Give the extent of all uninfected red blood cells.
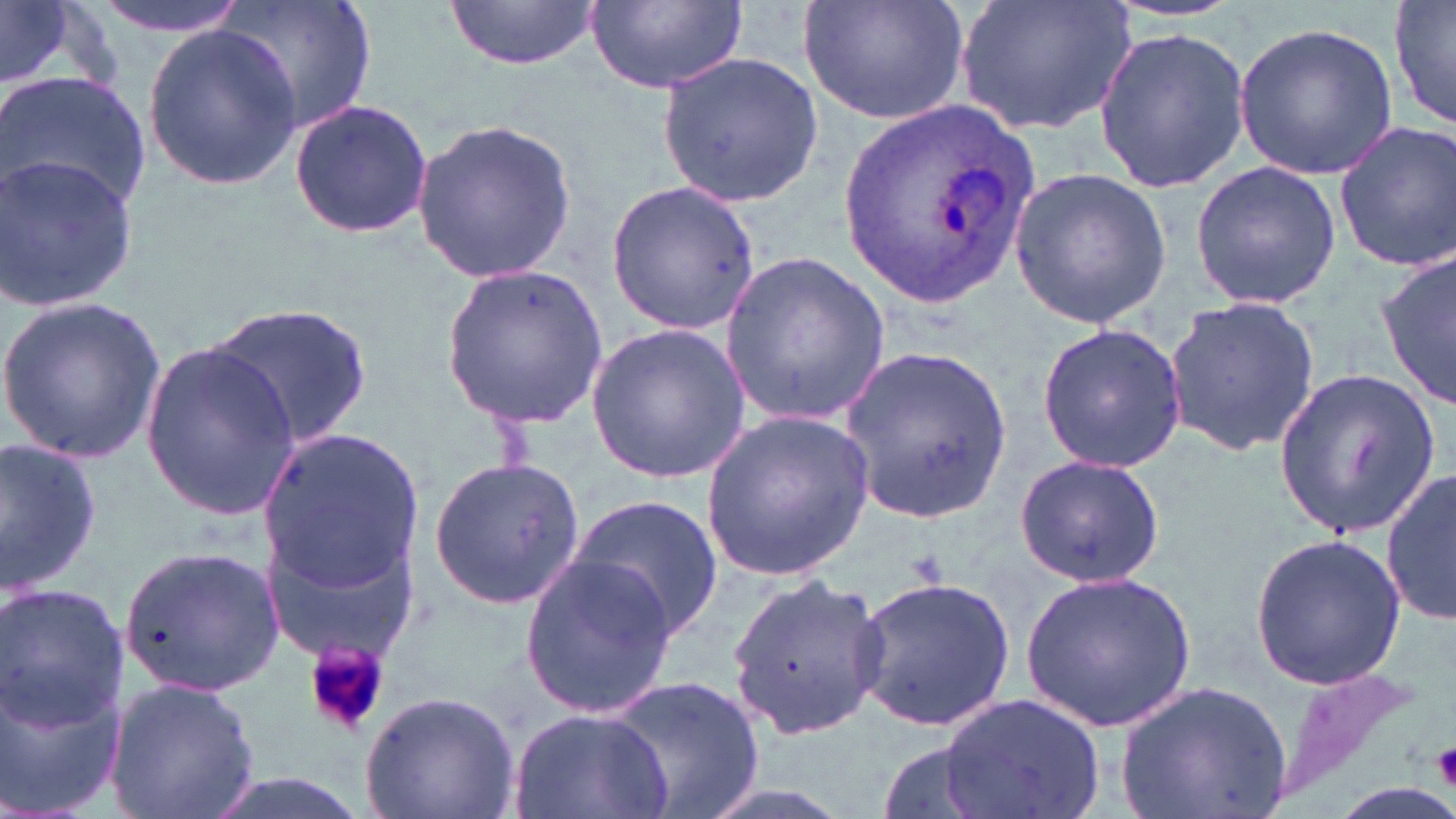
Approximate bounding boxes as (x1, y1, x2, y2) in pixels.
Uninfected red blood cells: (88, 0, 250, 38), (220, 0, 378, 135), (587, 0, 747, 91), (798, 0, 973, 126), (957, 0, 1137, 137), (1390, 0, 1455, 133), (444, 1, 602, 73), (0, 3, 103, 94), (1235, 21, 1398, 180), (141, 22, 302, 189), (1093, 26, 1251, 191), (656, 52, 822, 205), (1, 72, 153, 214), (287, 97, 435, 241), (412, 117, 578, 282), (1331, 120, 1456, 272), (0, 151, 138, 316), (1190, 162, 1341, 309), (1008, 167, 1174, 329), (605, 179, 761, 334), (1378, 247, 1456, 410), (720, 249, 890, 423), (440, 264, 607, 424), (1163, 293, 1321, 458), (0, 294, 166, 461), (209, 302, 375, 450), (587, 323, 751, 482), (1035, 323, 1187, 474), (139, 343, 304, 519), (843, 346, 1012, 522), (1273, 366, 1440, 538), (701, 409, 872, 582), (259, 430, 422, 590), (0, 433, 101, 596), (429, 453, 586, 610), (1012, 454, 1166, 588), (1382, 468, 1454, 627), (567, 490, 725, 644), (262, 519, 416, 659), (1248, 533, 1407, 690), (118, 544, 288, 699), (517, 550, 677, 721), (1022, 571, 1195, 730), (726, 572, 891, 738), (852, 575, 1018, 732), (0, 585, 129, 731), (0, 673, 127, 819), (606, 676, 767, 819), (109, 677, 263, 819), (1115, 678, 1292, 819), (358, 689, 521, 819), (939, 692, 1105, 819), (510, 704, 672, 819), (874, 736, 994, 819), (193, 770, 379, 819).

slide-level diagnosis = Plasmodium ovale
magnification = 1000x
Plasmodium ovale-infected red blood cell locations = approximate bounding boxes as (x1, y1, x2, y2) in pixels: (838, 102, 1035, 309)
modality = optical microscopy
field of view = single
stain = May-Grünwald-Giemsa
platelet locations = approximate bounding boxes as (x1, y1, x2, y2) in pixels: (304, 639, 394, 738), (1430, 743, 1456, 786)
image size = 1456×819 pixels
preparation = thin blood film